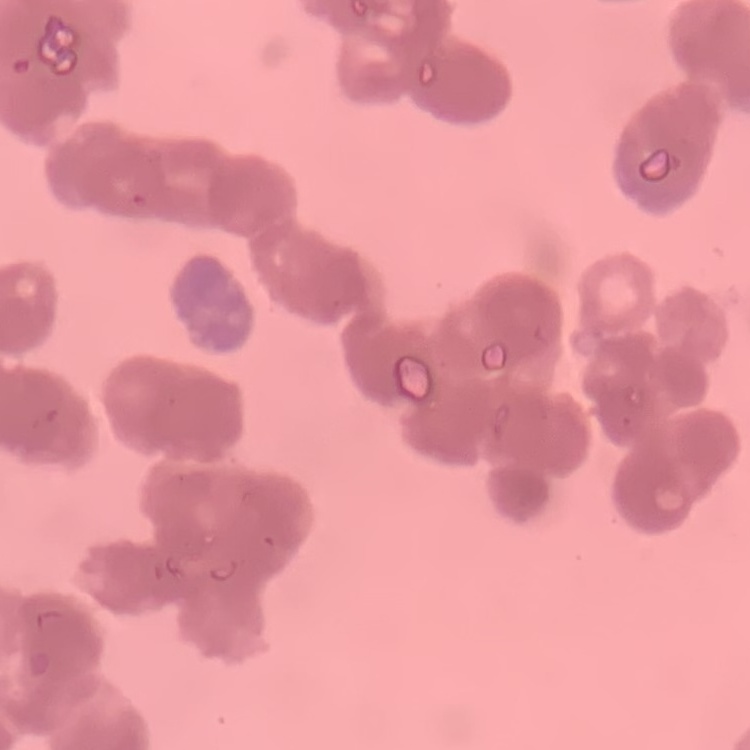

red blood cell morphology = rouleaux formation
stain = Field's or Giemsa
image type = one tile cut from a larger photomicrograph
preparation = thin peripheral smear